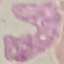
Malaria status: uninfected. Automatically extracted cell patch, resized to 64 × 64 pixels. Acquired by smartphone through the microscope eyepiece. Thin blood film. Giemsa stain.